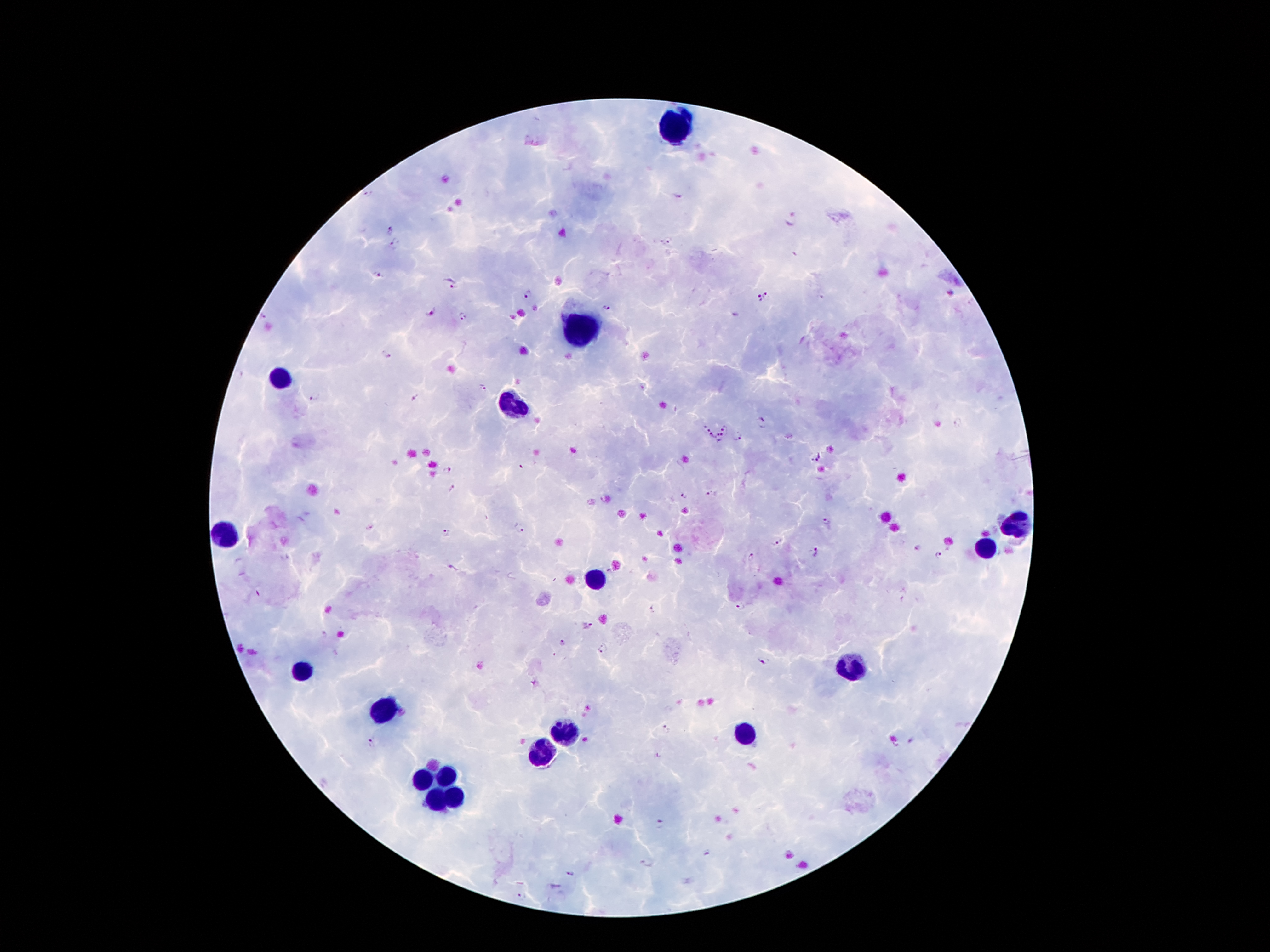
Approximate centers as [x, y] in pixels.
Summary:
  - Leukocyte locations: [672, 127], [577, 330], [281, 379], [512, 407], [1016, 522], [225, 535], [986, 547], [594, 581], [850, 666], [304, 669], [384, 713], [563, 731], [745, 733], [542, 754], [449, 775], [422, 783], [453, 797], [435, 799]
  - Malaria parasite locations: [369, 195], [791, 216], [389, 230], [395, 245], [667, 245], [378, 276], [455, 286], [768, 292], [528, 294], [758, 300], [606, 309], [431, 313], [266, 317], [463, 318], [386, 355], [484, 388], [313, 398], [415, 399], [958, 424], [705, 428], [725, 428], [711, 436], [738, 436], [722, 438], [815, 457], [447, 470], [452, 489], [711, 494], [683, 495], [827, 524], [520, 528], [447, 532], [778, 540], [814, 553], [939, 556], [752, 557], [739, 607], [656, 609], [587, 625], [563, 643], [603, 648], [765, 660], [668, 730], [369, 742], [661, 826], [705, 854], [648, 861], [570, 874], [522, 895]
  - Capture: smartphone camera through the microscope eyepiece
  - Stain: Giemsa
  - Patient malaria status: positive for Plasmodium falciparum
  - Magnification: 100x
  - Preparation: thick blood film
  - Image size: 1270×952 pixels
  - Field of view: one from this slide